Give the extent of all Trypanosoma brucei.
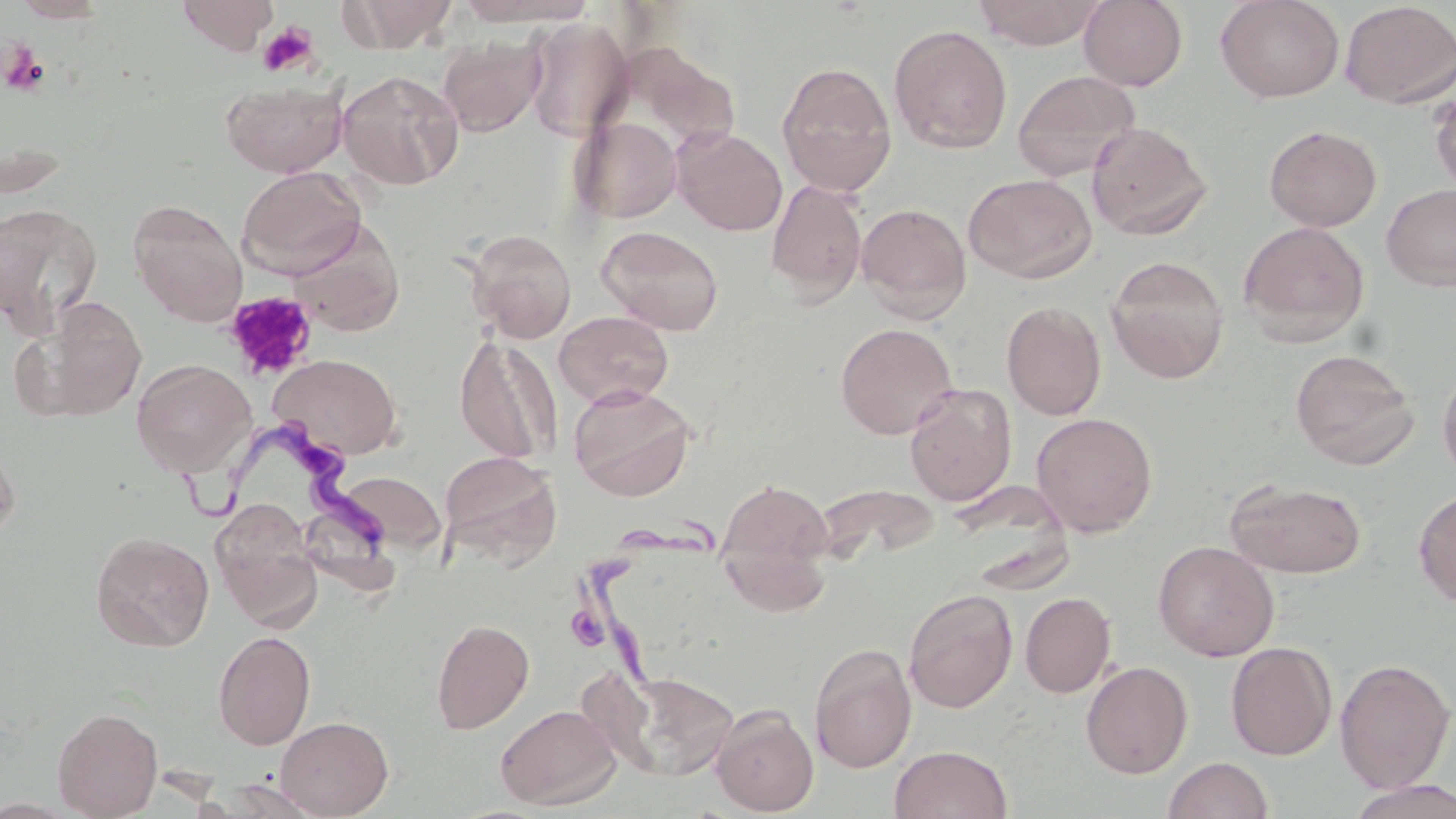
Approximate bounding boxes as (x1, y1, x2, y2) in pixels.
Trypanosoma brucei: (162, 415, 386, 554), (578, 518, 713, 706).

Platelet locations: (257, 22, 320, 77), (0, 41, 49, 96), (223, 290, 317, 381). Uninfected red blood cell locations: (10, 0, 113, 23), (177, 0, 278, 53), (342, 0, 459, 52), (453, 0, 595, 27), (971, 0, 1106, 49), (1078, 0, 1188, 91), (1215, 0, 1344, 103), (1339, 1, 1456, 109), (524, 19, 633, 142), (889, 24, 1013, 154), (438, 35, 545, 136), (776, 61, 897, 197), (1012, 69, 1140, 182), (336, 70, 464, 190), (220, 78, 348, 177), (1430, 87, 1456, 194), (571, 116, 682, 224), (1086, 121, 1211, 240), (1263, 125, 1382, 232), (673, 127, 787, 236), (237, 165, 366, 277), (964, 173, 1097, 283), (766, 180, 867, 306), (1381, 183, 1456, 291), (128, 199, 248, 326), (0, 203, 103, 331), (856, 203, 972, 321), (1238, 221, 1370, 345), (596, 225, 724, 335), (466, 228, 577, 343), (1105, 255, 1230, 383), (13, 296, 148, 423), (1001, 301, 1106, 421), (554, 311, 673, 409), (835, 322, 958, 439), (454, 334, 560, 464), (1290, 349, 1419, 469), (269, 353, 403, 459), (131, 359, 256, 476), (1437, 364, 1456, 485), (568, 384, 696, 502), (904, 384, 1016, 506), (1030, 412, 1157, 537), (0, 435, 20, 546), (439, 451, 562, 567), (335, 471, 446, 553), (716, 477, 836, 607), (1225, 479, 1367, 579), (1413, 488, 1456, 608), (211, 500, 323, 629), (90, 532, 214, 652), (1153, 540, 1279, 661), (904, 588, 1018, 713), (1020, 591, 1116, 697), (431, 618, 534, 733), (213, 630, 316, 750), (1226, 642, 1337, 760), (808, 643, 917, 772), (1334, 658, 1454, 793), (1080, 660, 1193, 778), (604, 670, 740, 781), (495, 703, 620, 810), (710, 704, 819, 816), (52, 707, 163, 818), (275, 716, 394, 818), (889, 745, 1013, 819), (1162, 756, 1274, 819), (220, 777, 325, 818), (1343, 779, 1456, 819). Slide-level diagnosis: Trypanosoma brucei. Light microscopy. Image is 1456×819 pixels. Single field of view. Thin blood film. Captured at 1000x magnification. May-Grünwald-Giemsa stain.